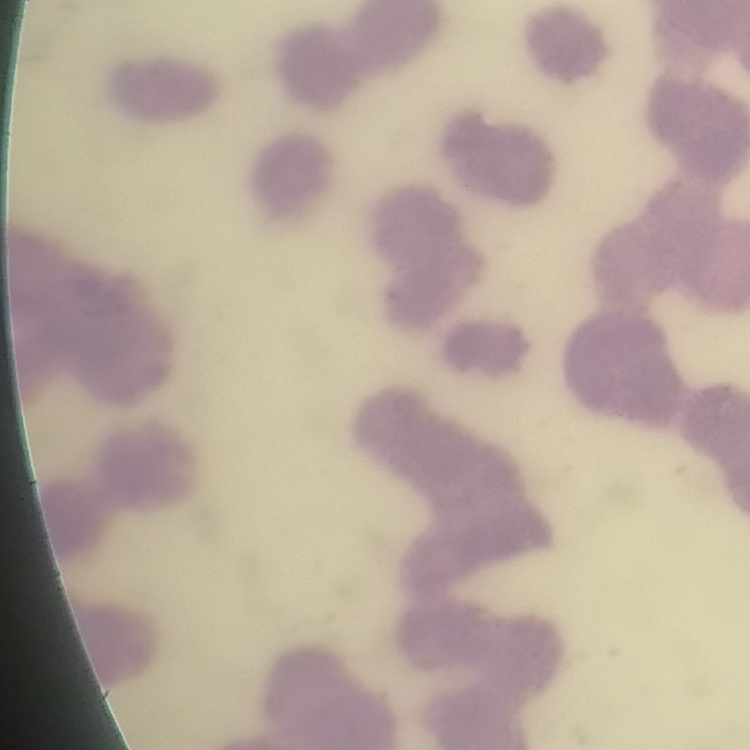
Summary:
  - Erythrocyte morphology: rouleaux formation
  - Stain: Field's or Giemsa
  - Image type: square crop of a larger photomicrograph
  - Preparation: thin blood film